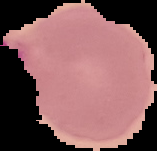

Segmented cell region on a black background. From a thin blood film. Malaria status: parasitized. Image is 157×151 pixels.